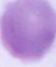

Micrograph. A red blood cell is shown. Captured at 1000x magnification.